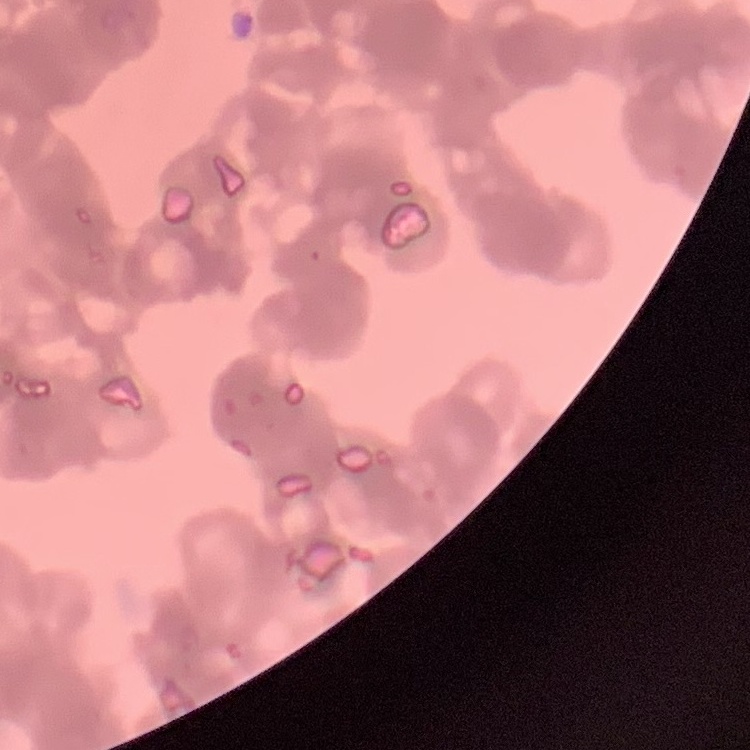
Summary:
  - Red blood cell morphology: rouleaux formation
  - Stain: Field's or Giemsa
  - Image type: one tile cut from a larger photomicrograph
  - Preparation: thin blood film